Comment on the morphology of the red blood cells.
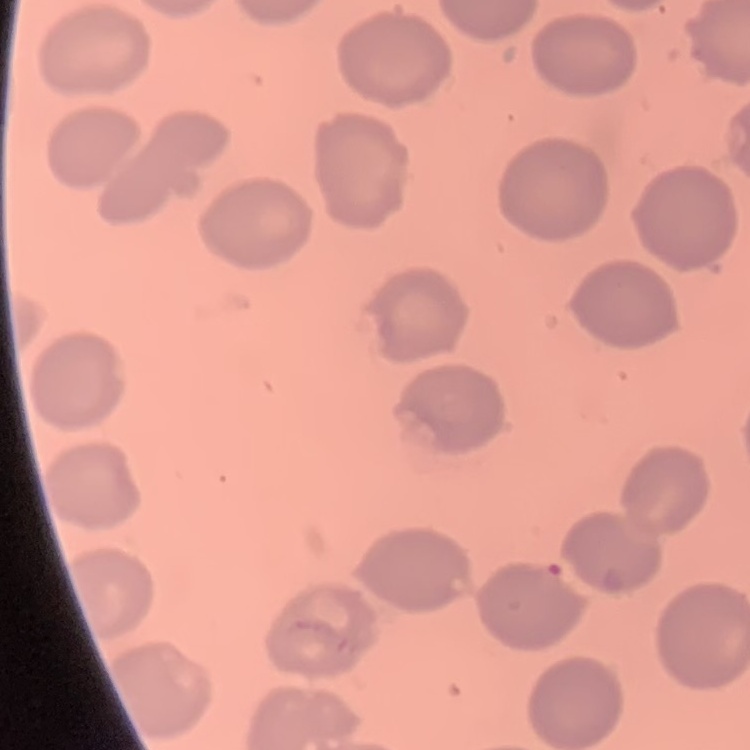
They show no rouleaux formation.

stain = Field's or Giemsa
image type = square crop of a larger photomicrograph
preparation = thin peripheral smear